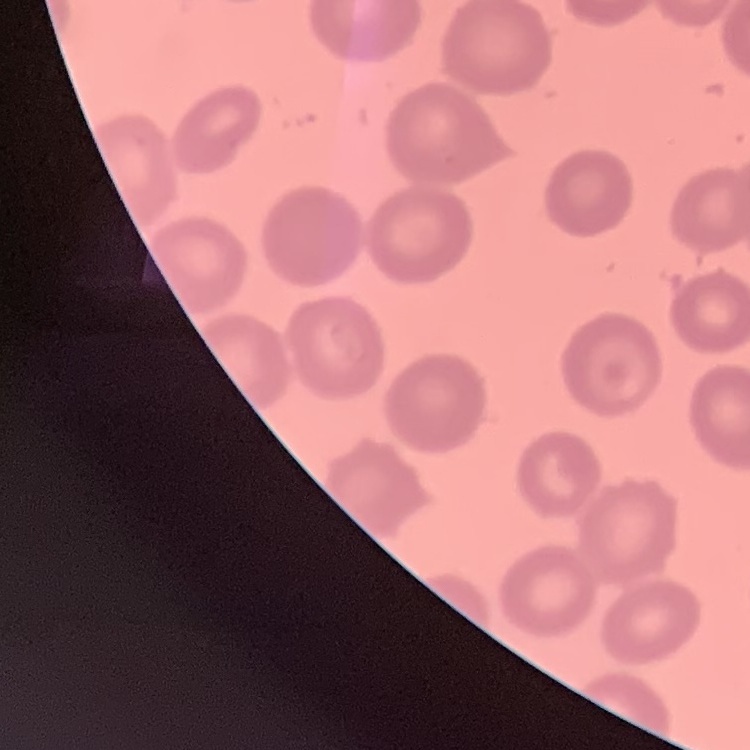
Summary:
  - Erythrocyte morphology: no rouleaux formation
  - Stain: Field's or Giemsa
  - Preparation: thin blood smear
  - Image type: one tile cut from a larger photomicrograph